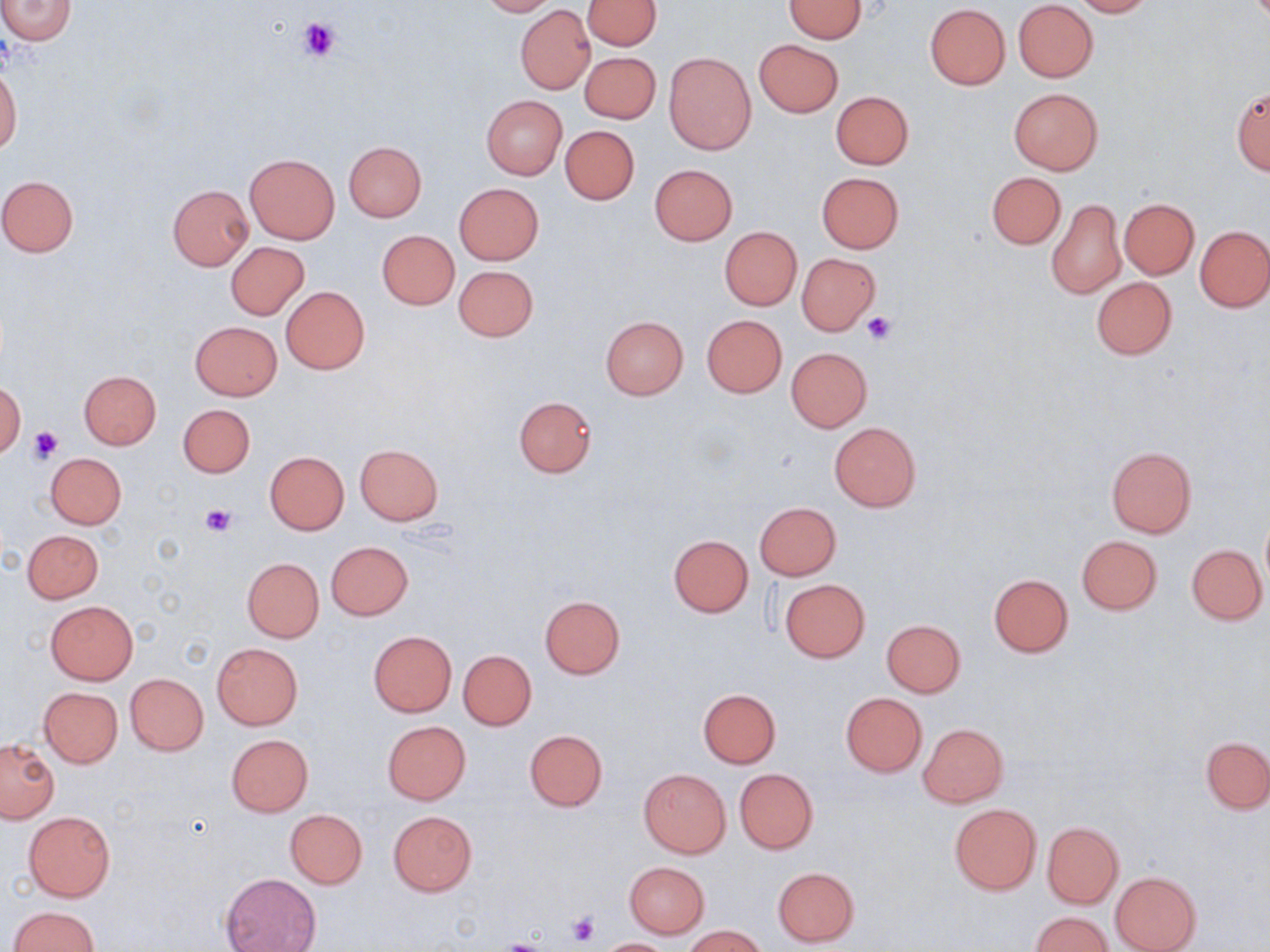

Approximate bounding boxes as named x1/y1/x2/y2 corners in pixels. Uninfected red blood cell locations: (x1=0, y1=0, x2=76, y2=44), (x1=478, y1=0, x2=556, y2=16), (x1=582, y1=0, x2=661, y2=51), (x1=784, y1=0, x2=868, y2=42), (x1=1072, y1=0, x2=1156, y2=17), (x1=1013, y1=1, x2=1098, y2=81), (x1=925, y1=4, x2=1011, y2=89), (x1=515, y1=6, x2=594, y2=93), (x1=754, y1=39, x2=843, y2=117), (x1=664, y1=51, x2=756, y2=154), (x1=579, y1=52, x2=660, y2=124), (x1=0, y1=64, x2=21, y2=157), (x1=1007, y1=86, x2=1104, y2=176), (x1=1231, y1=86, x2=1270, y2=175), (x1=830, y1=91, x2=914, y2=169), (x1=481, y1=95, x2=567, y2=180), (x1=561, y1=125, x2=639, y2=204), (x1=342, y1=140, x2=426, y2=222), (x1=245, y1=153, x2=340, y2=243), (x1=650, y1=163, x2=738, y2=245), (x1=816, y1=172, x2=904, y2=253), (x1=986, y1=172, x2=1065, y2=250), (x1=0, y1=176, x2=79, y2=257), (x1=453, y1=183, x2=543, y2=266), (x1=168, y1=184, x2=253, y2=269), (x1=1047, y1=198, x2=1125, y2=299), (x1=1119, y1=198, x2=1199, y2=279), (x1=1196, y1=225, x2=1270, y2=312), (x1=720, y1=228, x2=802, y2=310), (x1=377, y1=230, x2=459, y2=310), (x1=226, y1=242, x2=309, y2=320), (x1=796, y1=253, x2=881, y2=335), (x1=453, y1=265, x2=538, y2=342), (x1=1091, y1=277, x2=1177, y2=359), (x1=281, y1=286, x2=369, y2=374), (x1=701, y1=314, x2=787, y2=397), (x1=600, y1=315, x2=689, y2=399), (x1=190, y1=321, x2=282, y2=400), (x1=786, y1=347, x2=871, y2=432), (x1=78, y1=370, x2=162, y2=449), (x1=0, y1=383, x2=24, y2=458), (x1=514, y1=396, x2=597, y2=477), (x1=179, y1=404, x2=256, y2=478), (x1=830, y1=421, x2=921, y2=512), (x1=354, y1=444, x2=443, y2=524), (x1=1105, y1=446, x2=1197, y2=538), (x1=265, y1=451, x2=348, y2=534), (x1=45, y1=452, x2=127, y2=529), (x1=755, y1=502, x2=840, y2=580), (x1=1261, y1=515, x2=1270, y2=591), (x1=22, y1=529, x2=104, y2=603), (x1=668, y1=534, x2=753, y2=616), (x1=1077, y1=535, x2=1161, y2=614), (x1=325, y1=541, x2=413, y2=620), (x1=1187, y1=544, x2=1267, y2=624), (x1=242, y1=558, x2=324, y2=642), (x1=988, y1=573, x2=1074, y2=657), (x1=780, y1=579, x2=870, y2=662), (x1=540, y1=596, x2=625, y2=678), (x1=45, y1=601, x2=138, y2=684), (x1=881, y1=620, x2=965, y2=697), (x1=368, y1=631, x2=457, y2=716), (x1=212, y1=643, x2=302, y2=729), (x1=458, y1=649, x2=536, y2=730), (x1=125, y1=673, x2=208, y2=756), (x1=39, y1=687, x2=123, y2=767), (x1=698, y1=689, x2=780, y2=768), (x1=841, y1=693, x2=927, y2=776), (x1=382, y1=720, x2=470, y2=804), (x1=918, y1=723, x2=1008, y2=806), (x1=525, y1=729, x2=608, y2=811), (x1=226, y1=734, x2=314, y2=816), (x1=1201, y1=735, x2=1270, y2=814), (x1=0, y1=740, x2=59, y2=822), (x1=639, y1=768, x2=730, y2=858), (x1=734, y1=768, x2=819, y2=853), (x1=949, y1=803, x2=1041, y2=895), (x1=285, y1=809, x2=367, y2=889), (x1=23, y1=810, x2=115, y2=901), (x1=388, y1=810, x2=477, y2=896), (x1=1041, y1=821, x2=1124, y2=909), (x1=624, y1=862, x2=709, y2=937), (x1=771, y1=866, x2=859, y2=947), (x1=1110, y1=871, x2=1201, y2=952), (x1=221, y1=873, x2=320, y2=952), (x1=9, y1=906, x2=99, y2=952), (x1=1031, y1=912, x2=1113, y2=951), (x1=684, y1=926, x2=767, y2=952), (x1=594, y1=938, x2=678, y2=951). Platelet locations: (x1=297, y1=16, x2=342, y2=61), (x1=862, y1=312, x2=894, y2=345), (x1=29, y1=424, x2=63, y2=461), (x1=201, y1=504, x2=236, y2=536), (x1=566, y1=911, x2=601, y2=947), (x1=498, y1=939, x2=549, y2=952). Slide-level diagnosis: no evidence of blood parasites. Light microscopy. May-Grünwald-Giemsa stain. Single field of view. 1000x magnification. Thin blood smear. Image is 1270×952 pixels.